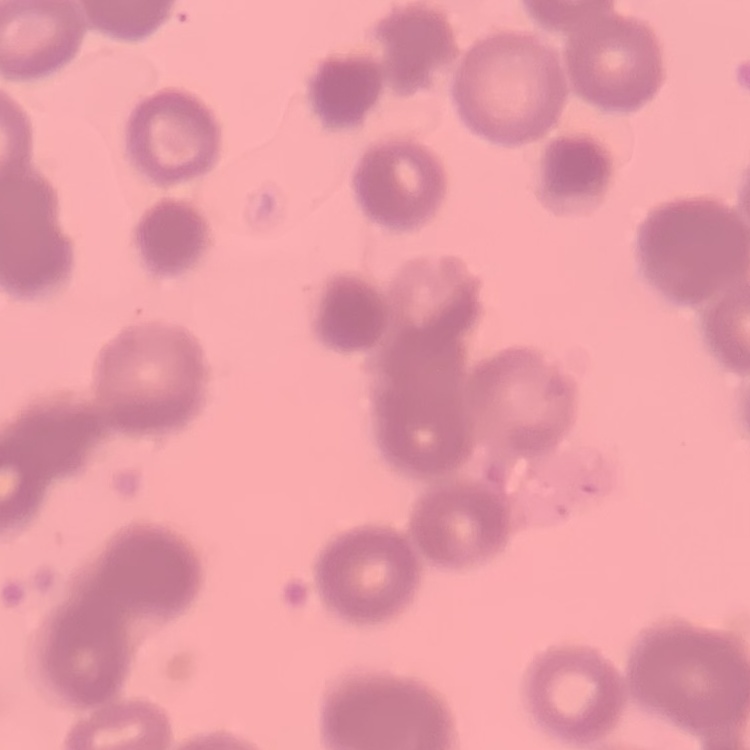
Summary:
  - Erythrocyte morphology: rouleaux formation
  - Preparation: thin blood film
  - Stain: Field's or Giemsa
  - Image type: square crop of a larger photomicrograph